Name the parasite shown.
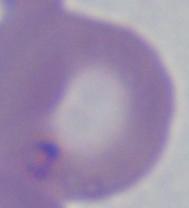
Babesia.

Summary:
  - Modality: micrograph
  - Magnification: 1000x